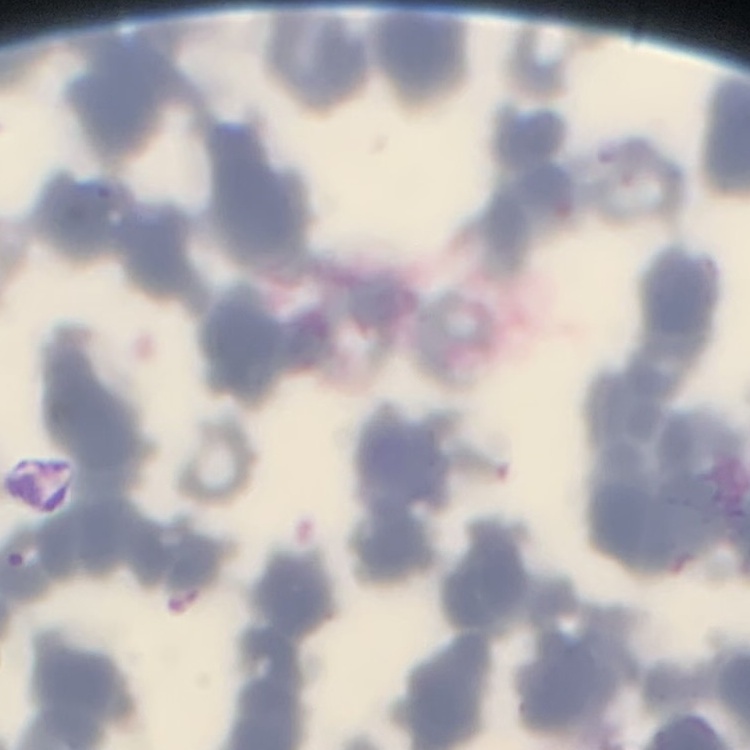 The erythrocytes exhibit rouleaux formation. One tile cut from a larger photomicrograph. Field's or Giemsa stain. Thin blood smear.